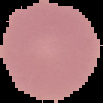
Result: no malaria parasites detected. From a thin blood film. The area outside the segmented cell region is set to black. Image is 103×103 pixels.